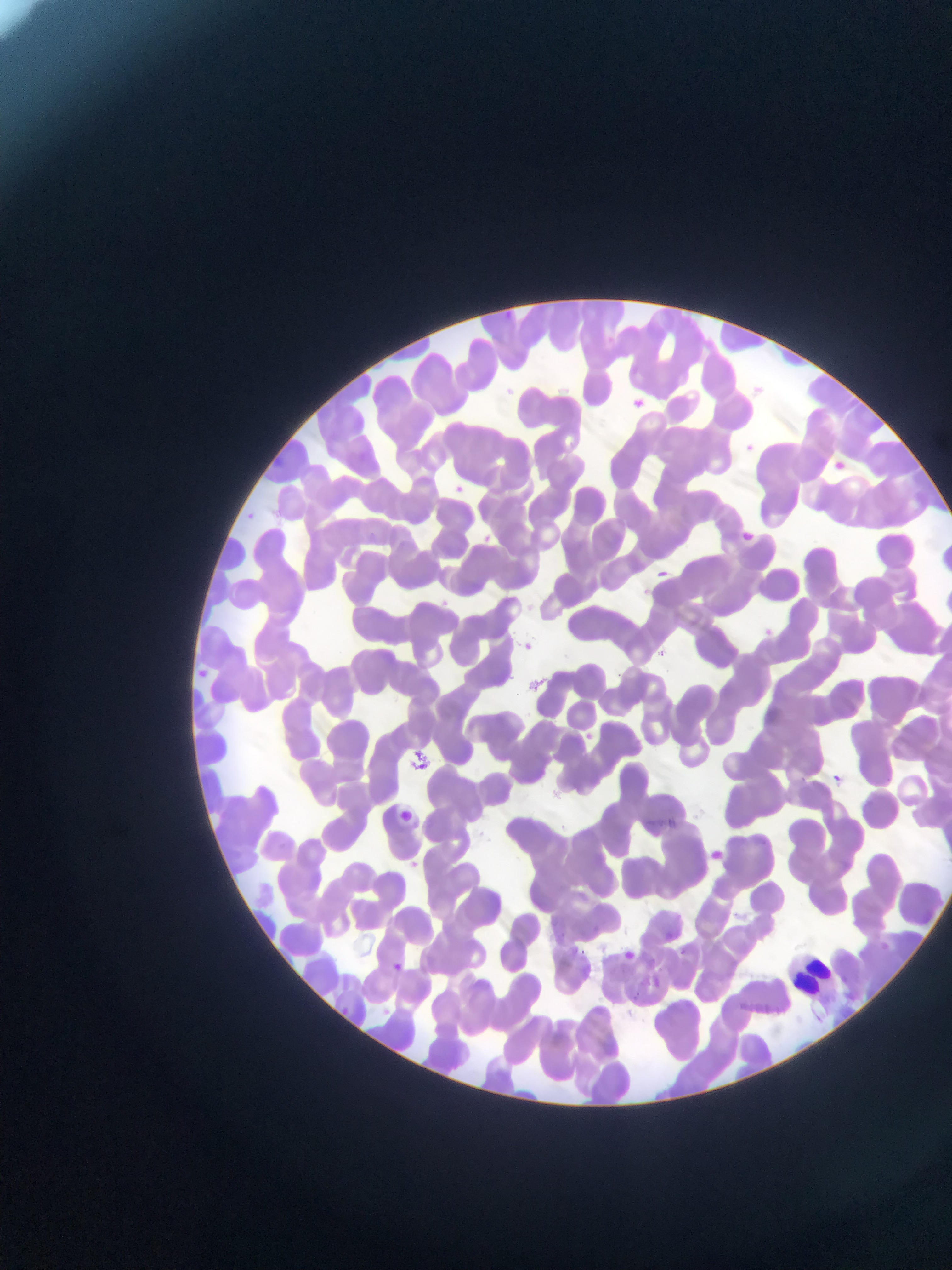 Approximate bounding boxes as [left, top, right, bottom] in pixels. Plasmodium parasite locations: [634, 396, 659, 417], [743, 433, 760, 458], [833, 455, 853, 472], [451, 483, 471, 496], [744, 526, 765, 546], [659, 566, 676, 579], [760, 621, 788, 651], [523, 638, 540, 655], [196, 664, 208, 679], [826, 771, 844, 783], [398, 805, 415, 822], [710, 845, 733, 869], [412, 856, 429, 868], [620, 949, 635, 964], [648, 951, 655, 960], [393, 959, 409, 977], [639, 975, 668, 984], [343, 1004, 360, 1020]. Leukocyte locations: [785, 948, 841, 1003]. Single field of view. Collected in Ghana. Photographed through a microscope with a mobile-phone camera. Thin blood film. Image is 952×1270 pixels.